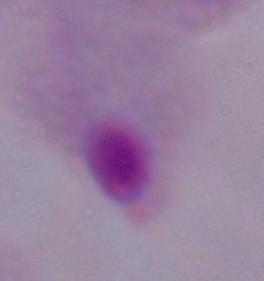

Summary:
  - Modality: photomicrograph
  - Magnification: 1000x
  - Identification: trichomonad